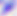
{
  "identification": "Toxoplasma gondii",
  "magnification": "400x",
  "modality": "micrograph"
}